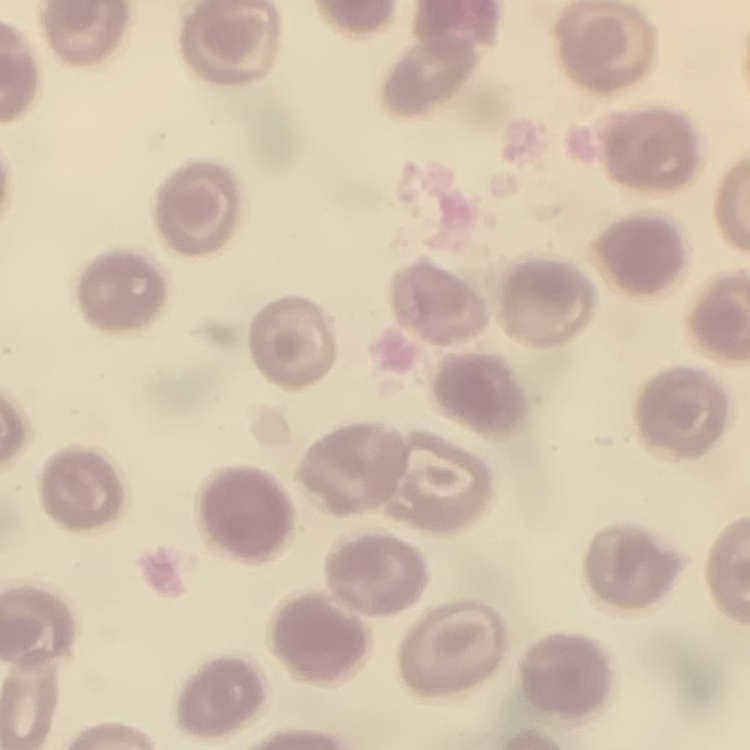
red blood cell morphology = no rouleaux formation
stain = Field's or Giemsa
preparation = thin blood smear
image type = square crop of a larger photomicrograph